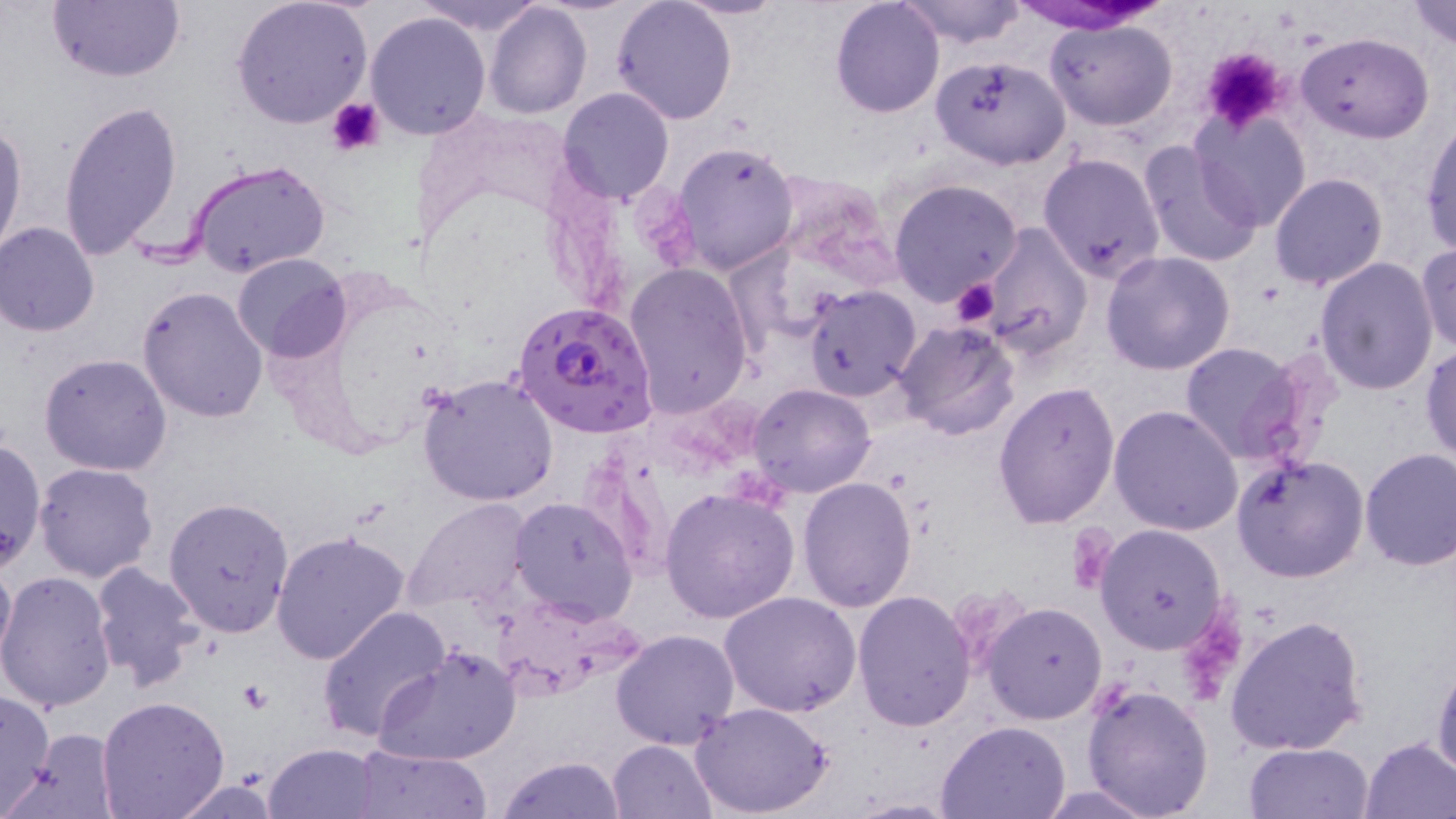
slide_level_diagnosis: Plasmodium falciparum
modality: optical microscopy
field_of_view: one of a larger specimen
plasmodium_falciparum_infected_red_blood_cell_locations: 'approximate bounding boxes as [x1, y1, x2, y2] in pixels: [512, 298, 657, 437]'
platelet_locations: 'approximate bounding boxes as [x1, y1, x2, y2] in pixels: [1198, 45, 1291, 135], [326, 97, 388, 159], [950, 278, 1000, 329], [1066, 528, 1116, 593]'
uninfected_red_blood_cell_locations: 'approximate bounding boxes as [x1, y1, x2, y2] in pixels: [48, 0, 187, 83], [417, 0, 546, 35], [611, 0, 738, 126], [830, 0, 944, 117], [897, 0, 1026, 49], [1407, 0, 1456, 48], [232, 1, 375, 132], [675, 1, 791, 21], [483, 2, 592, 119], [364, 10, 493, 140], [1045, 19, 1178, 131], [1296, 31, 1434, 142], [928, 55, 1073, 171], [556, 86, 674, 206], [58, 99, 183, 261], [1190, 109, 1312, 233], [0, 118, 27, 256], [1420, 120, 1455, 258], [671, 138, 801, 275], [1137, 140, 1263, 270], [1038, 153, 1165, 282], [187, 159, 331, 280], [768, 169, 900, 284], [1269, 173, 1390, 290], [888, 177, 1024, 305], [1, 222, 100, 337], [975, 222, 1092, 357], [1418, 244, 1456, 353], [1101, 251, 1236, 375], [233, 252, 351, 364], [1314, 258, 1439, 395], [622, 264, 753, 421], [803, 284, 922, 402], [137, 287, 270, 424], [891, 320, 1020, 440], [1176, 342, 1313, 464], [1421, 344, 1456, 464], [40, 352, 173, 476], [418, 374, 560, 506], [992, 380, 1121, 529], [747, 382, 875, 497], [1108, 405, 1242, 536], [1, 444, 46, 571], [1359, 447, 1456, 570], [1229, 453, 1371, 583], [33, 462, 159, 584], [798, 477, 919, 612], [659, 486, 799, 623], [163, 496, 296, 636], [508, 496, 637, 624], [405, 499, 532, 615], [1095, 522, 1228, 653], [270, 531, 411, 664], [0, 546, 15, 678], [88, 561, 205, 689], [0, 571, 117, 714], [852, 589, 977, 731], [719, 592, 862, 717], [981, 601, 1108, 724], [315, 604, 451, 744], [1225, 614, 1369, 755], [612, 628, 741, 750], [374, 644, 521, 766], [1431, 657, 1456, 780], [1082, 681, 1215, 818], [0, 690, 56, 813], [96, 695, 231, 819], [691, 701, 835, 818], [938, 720, 1071, 818], [14, 728, 121, 817], [1359, 738, 1456, 818], [609, 739, 720, 819], [265, 742, 382, 817], [1243, 742, 1374, 819], [351, 743, 492, 818], [496, 754, 626, 819], [169, 777, 283, 817], [1037, 784, 1161, 818]'
magnification: 1000x
preparation: thin blood film
image_size: 1456×819 pixels
white_blood_cell_locations: 'approximate bounding boxes as [x1, y1, x2, y2] in pixels: [1009, 0, 1169, 32]'
stain: May-Grünwald-Giemsa